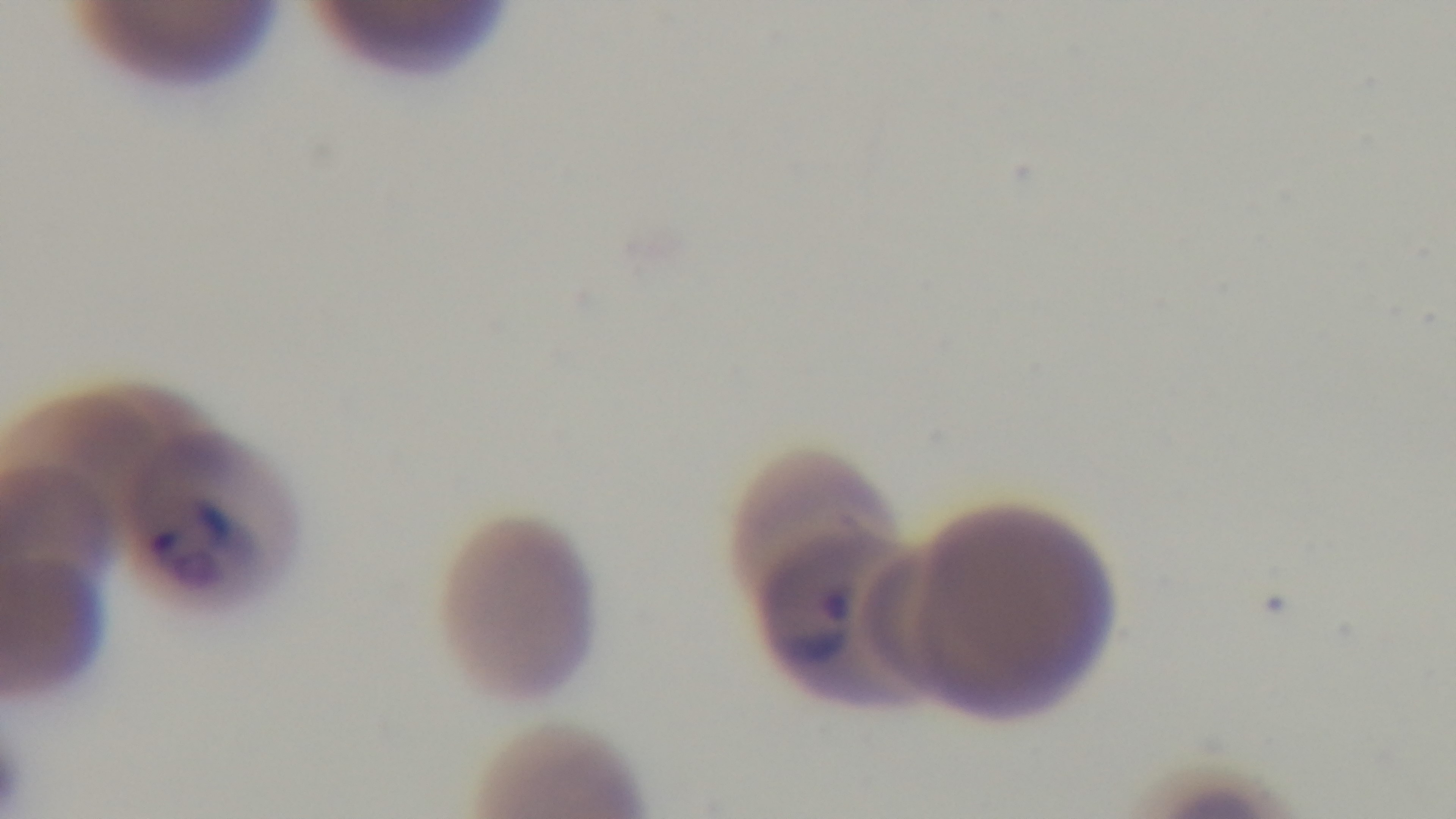

Malaria status: positive. Single field of view. Mounted 4K digital camera. Light microscopy. Preparation: thin. 100x oil-immersion objective. Giemsa-stained.